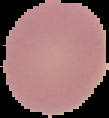

From a thin blood film. Result: negative for malaria parasites. Cell region segmented out of the field of view; the surrounding area is masked to black. Image is 109×118 pixels.